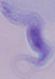

Photomicrograph. 1000x magnification. A trypanosome is seen.